Give the extent of all Trypanosoma brucei.
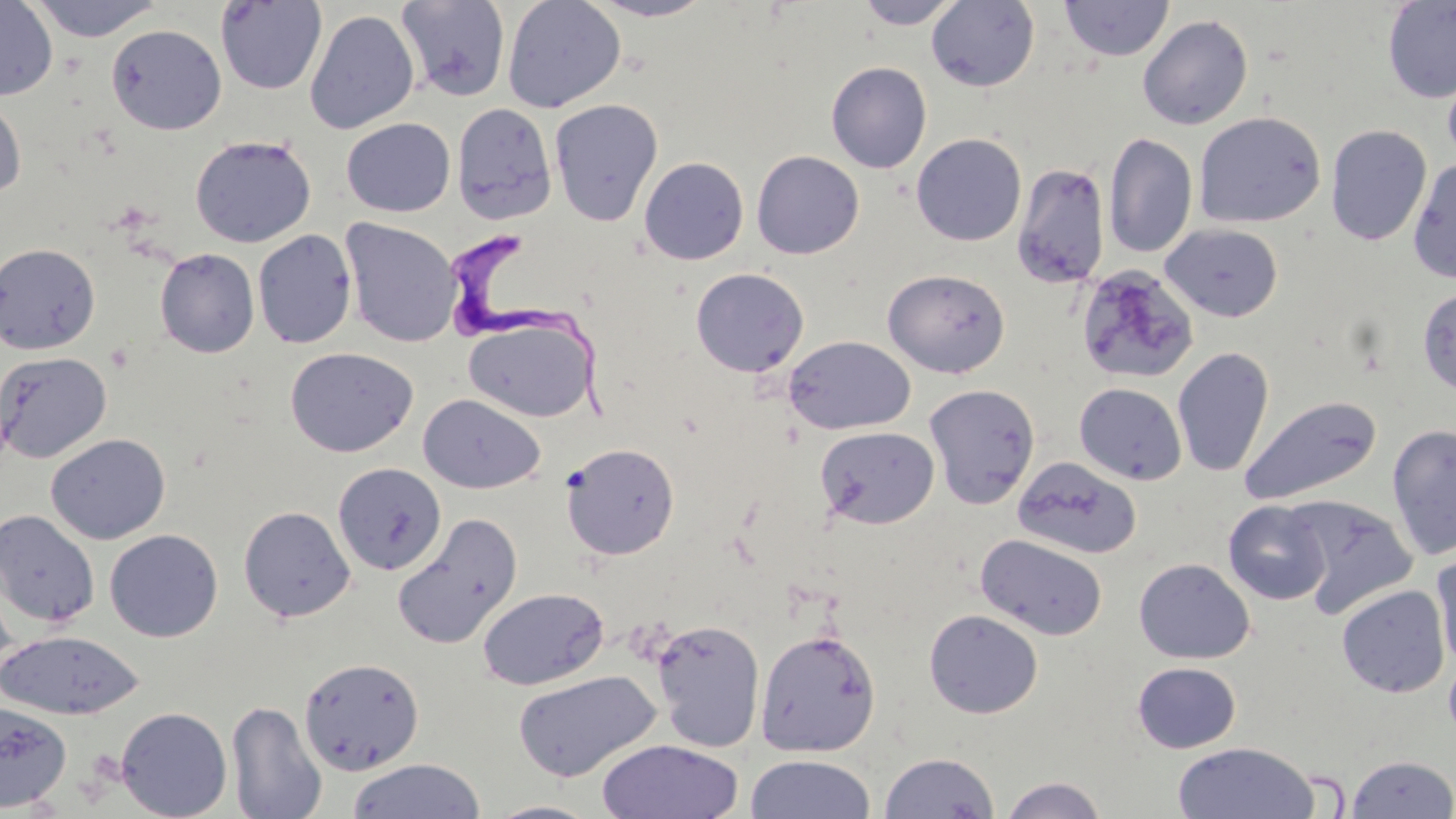
Approximate bounding boxes as named x1/y1/x2/y2 corners in pixels.
Trypanosoma brucei: (x1=448, y1=232, x2=623, y2=427).

Summary:
  - Uninfected red blood cell locations: (x1=0, y1=0, x2=58, y2=101), (x1=27, y1=0, x2=165, y2=42), (x1=502, y1=0, x2=626, y2=113), (x1=585, y1=0, x2=719, y2=22), (x1=854, y1=0, x2=963, y2=30), (x1=1059, y1=0, x2=1173, y2=61), (x1=215, y1=1, x2=327, y2=95), (x1=395, y1=1, x2=512, y2=102), (x1=927, y1=1, x2=1040, y2=92), (x1=1382, y1=1, x2=1456, y2=103), (x1=304, y1=9, x2=420, y2=134), (x1=1137, y1=14, x2=1254, y2=130), (x1=105, y1=23, x2=227, y2=135), (x1=1441, y1=55, x2=1456, y2=172), (x1=825, y1=61, x2=932, y2=173), (x1=0, y1=94, x2=27, y2=200), (x1=549, y1=99, x2=664, y2=226), (x1=451, y1=102, x2=557, y2=224), (x1=1193, y1=111, x2=1326, y2=229), (x1=341, y1=118, x2=455, y2=217), (x1=1325, y1=124, x2=1432, y2=246), (x1=911, y1=133, x2=1027, y2=246), (x1=1103, y1=133, x2=1198, y2=258), (x1=190, y1=134, x2=316, y2=247), (x1=751, y1=150, x2=864, y2=259), (x1=639, y1=156, x2=749, y2=265), (x1=1407, y1=156, x2=1456, y2=284), (x1=1012, y1=162, x2=1110, y2=289), (x1=340, y1=218, x2=463, y2=348), (x1=1160, y1=223, x2=1283, y2=322), (x1=253, y1=229, x2=357, y2=348), (x1=0, y1=243, x2=101, y2=355), (x1=155, y1=248, x2=259, y2=358), (x1=1076, y1=264, x2=1198, y2=385), (x1=690, y1=267, x2=809, y2=378), (x1=882, y1=268, x2=1010, y2=378), (x1=1417, y1=286, x2=1456, y2=397), (x1=462, y1=315, x2=598, y2=424), (x1=783, y1=335, x2=916, y2=435), (x1=284, y1=346, x2=418, y2=458), (x1=1172, y1=347, x2=1274, y2=478), (x1=0, y1=351, x2=112, y2=463), (x1=1074, y1=382, x2=1188, y2=485), (x1=923, y1=383, x2=1040, y2=509), (x1=418, y1=393, x2=545, y2=494), (x1=1239, y1=395, x2=1383, y2=507), (x1=1386, y1=424, x2=1456, y2=560), (x1=814, y1=425, x2=939, y2=529), (x1=45, y1=433, x2=171, y2=544), (x1=561, y1=442, x2=680, y2=560), (x1=1013, y1=457, x2=1143, y2=560), (x1=332, y1=462, x2=446, y2=576), (x1=1288, y1=495, x2=1416, y2=617), (x1=1223, y1=500, x2=1331, y2=605), (x1=238, y1=505, x2=356, y2=622), (x1=0, y1=510, x2=99, y2=629), (x1=392, y1=513, x2=523, y2=650), (x1=104, y1=528, x2=223, y2=642), (x1=975, y1=532, x2=1108, y2=641), (x1=1431, y1=553, x2=1456, y2=671), (x1=1134, y1=558, x2=1255, y2=664), (x1=0, y1=580, x2=21, y2=689), (x1=1336, y1=584, x2=1451, y2=698), (x1=477, y1=587, x2=609, y2=691), (x1=924, y1=609, x2=1044, y2=719), (x1=649, y1=618, x2=765, y2=753), (x1=755, y1=628, x2=881, y2=757), (x1=0, y1=630, x2=145, y2=721), (x1=299, y1=657, x2=425, y2=776), (x1=1132, y1=661, x2=1242, y2=753), (x1=512, y1=669, x2=661, y2=782), (x1=226, y1=700, x2=327, y2=819), (x1=0, y1=701, x2=72, y2=812), (x1=116, y1=706, x2=232, y2=819), (x1=596, y1=738, x2=744, y2=819), (x1=1171, y1=742, x2=1320, y2=819), (x1=878, y1=750, x2=1001, y2=819), (x1=744, y1=753, x2=877, y2=819), (x1=1345, y1=754, x2=1456, y2=818), (x1=346, y1=758, x2=486, y2=819), (x1=999, y1=775, x2=1108, y2=819), (x1=484, y1=800, x2=603, y2=818)
  - Slide-level diagnosis: Trypanosoma brucei
  - Magnification: 1000x
  - Preparation: thin blood film
  - Modality: optical microscopy
  - Field of view: single
  - Image size: 1456×819 pixels
  - Stain: May-Grünwald-Giemsa